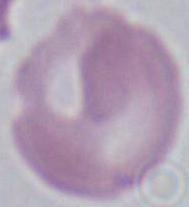
modality = photomicrograph
identification = red blood cell
magnification = 1000x